Locate every Plasmodium parasite.
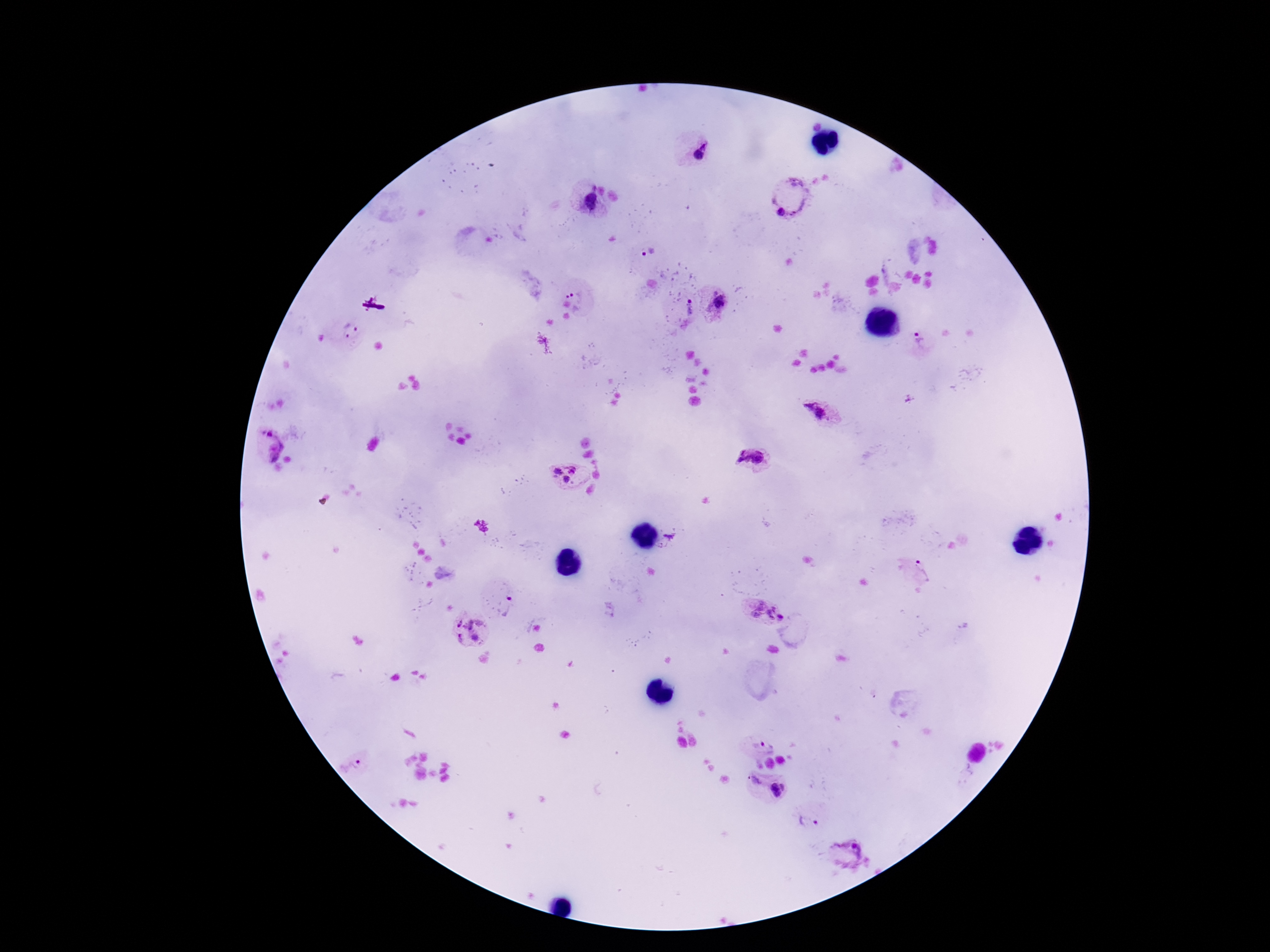
Approximate centers as [x, y] in pixels.
Plasmodium parasites: [697, 151], [592, 186], [791, 195], [590, 202], [781, 212], [648, 251], [713, 292], [578, 293], [720, 302], [574, 304], [689, 308], [350, 330], [922, 342], [819, 413], [269, 434], [273, 450], [753, 457], [572, 468], [556, 472], [566, 479], [667, 540], [913, 571], [498, 600], [766, 611], [466, 629], [351, 767], [753, 779], [779, 789], [805, 821], [846, 854].

patient malaria status = positive
preparation = thick blood smear
capture = smartphone camera through the microscope eyepiece
image size = 1270×952 pixels
field of view = single
stain = Giemsa
magnification = 100x